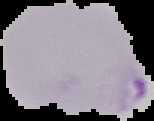
Malaria status: parasitized. Image is 154×121 pixels. Segmented cell region on a black background. From a thin blood smear.